Classify this cell by malaria status.
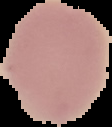

Uninfected.

preparation = thin blood smear
image size = 112×127 pixels
image type = cell region segmented out of the field of view; surrounding area masked to black